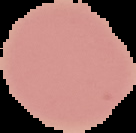

Summary:
  - Result: negative for malaria parasites
  - Preparation: thin blood smear
  - Image size: 136×133 pixels
  - Image type: cell region segmented out of the field of view; surrounding area masked to black